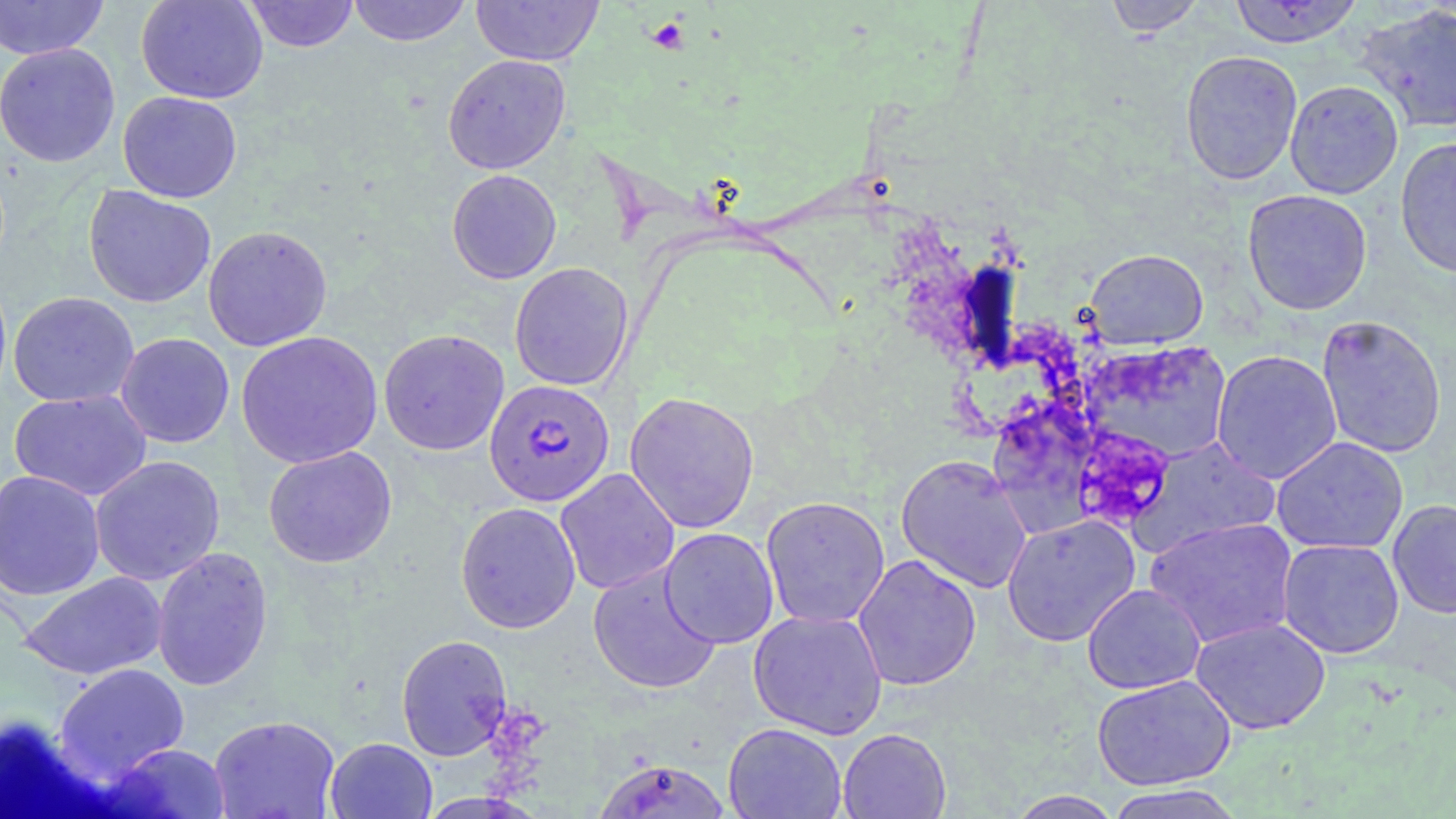

Approximate bounding boxes as (x1, y1, x2, y2) in pixels. Plasmodium falciparum-infected red blood cell locations: (484, 379, 615, 506). Platelet locations: (647, 15, 691, 53). Uninfected red blood cell locations: (0, 0, 109, 60), (135, 0, 268, 104), (243, 0, 359, 53), (347, 0, 472, 47), (471, 0, 604, 66), (1104, 0, 1206, 37), (1227, 1, 1365, 48), (1353, 3, 1455, 135), (0, 43, 121, 167), (1180, 50, 1303, 186), (442, 54, 570, 174), (1284, 80, 1404, 199), (117, 91, 242, 203), (1395, 137, 1456, 279), (446, 169, 562, 284), (83, 185, 216, 308), (1242, 189, 1372, 315), (203, 225, 333, 351), (1084, 248, 1209, 349), (509, 262, 634, 391), (8, 291, 139, 407), (1316, 314, 1447, 458), (378, 328, 509, 456), (236, 331, 383, 468), (115, 333, 235, 448), (1080, 340, 1235, 465), (1211, 349, 1342, 485), (9, 389, 152, 501), (624, 390, 760, 534), (1130, 436, 1281, 557), (1271, 436, 1408, 554), (263, 446, 397, 568), (895, 453, 1033, 593), (90, 455, 225, 585), (555, 468, 680, 595), (0, 469, 106, 601), (760, 496, 891, 629), (1388, 499, 1456, 618), (455, 501, 581, 633), (1002, 514, 1140, 646), (1144, 517, 1298, 649), (659, 527, 779, 649), (1277, 538, 1405, 659), (152, 546, 273, 691), (853, 554, 982, 691), (588, 564, 720, 695), (19, 572, 167, 680), (1082, 583, 1206, 694), (748, 609, 888, 740), (1190, 617, 1331, 735), (396, 634, 512, 761), (53, 663, 190, 781), (1091, 674, 1236, 790), (208, 714, 341, 819), (723, 722, 847, 819), (837, 727, 951, 818), (325, 737, 437, 819), (100, 742, 232, 818), (593, 757, 733, 818), (1103, 784, 1246, 819), (1007, 790, 1123, 818). Slide-level diagnosis: Plasmodium falciparum. Thin blood film. Optical microscopy. Captured at 1000x magnification. One field of a larger specimen. Image is 1456×819 pixels. May-Grünwald-Giemsa stain.